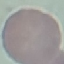

Malaria status: uninfected. Thin blood smear. Automatically extracted cell patch, resized to 64 × 64 pixels. Giemsa-stained preparation. Photographed with a smartphone camera at the microscope eyepiece.